Name the cell type shown.
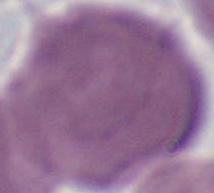

This is an erythrocyte.

Captured at 1000x magnification. Micrograph.